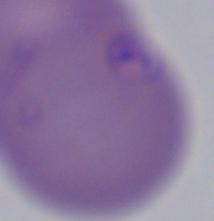 1000x magnification. Micrograph. A Babesia parasite is seen.